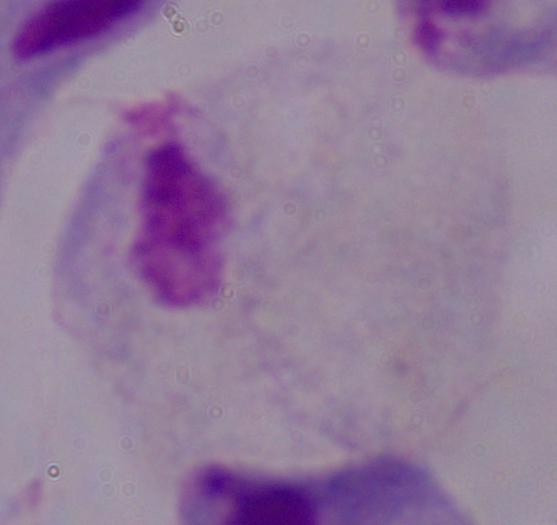
modality = photomicrograph
identification = trichomonad
magnification = 1000x